Classify this cell by malaria status.
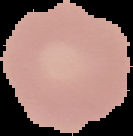
It is uninfected.

image size = 133×136 pixels
image type = segmented cell region with the area outside set to black
preparation = thin blood smear